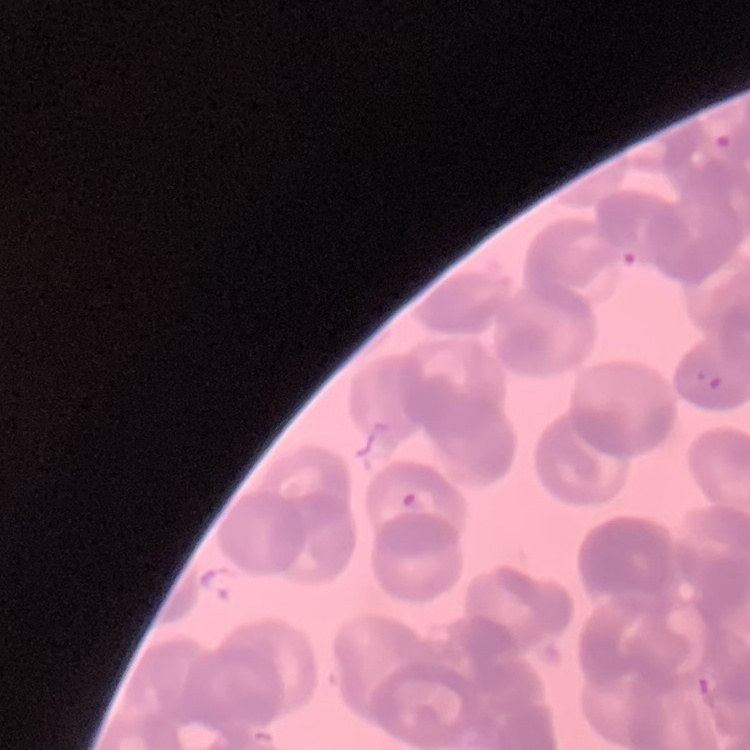

Summary:
  - Erythrocyte morphology: rouleaux formation
  - Preparation: thin blood film
  - Image type: one tile cut from a larger photomicrograph
  - Stain: Field's or Giemsa